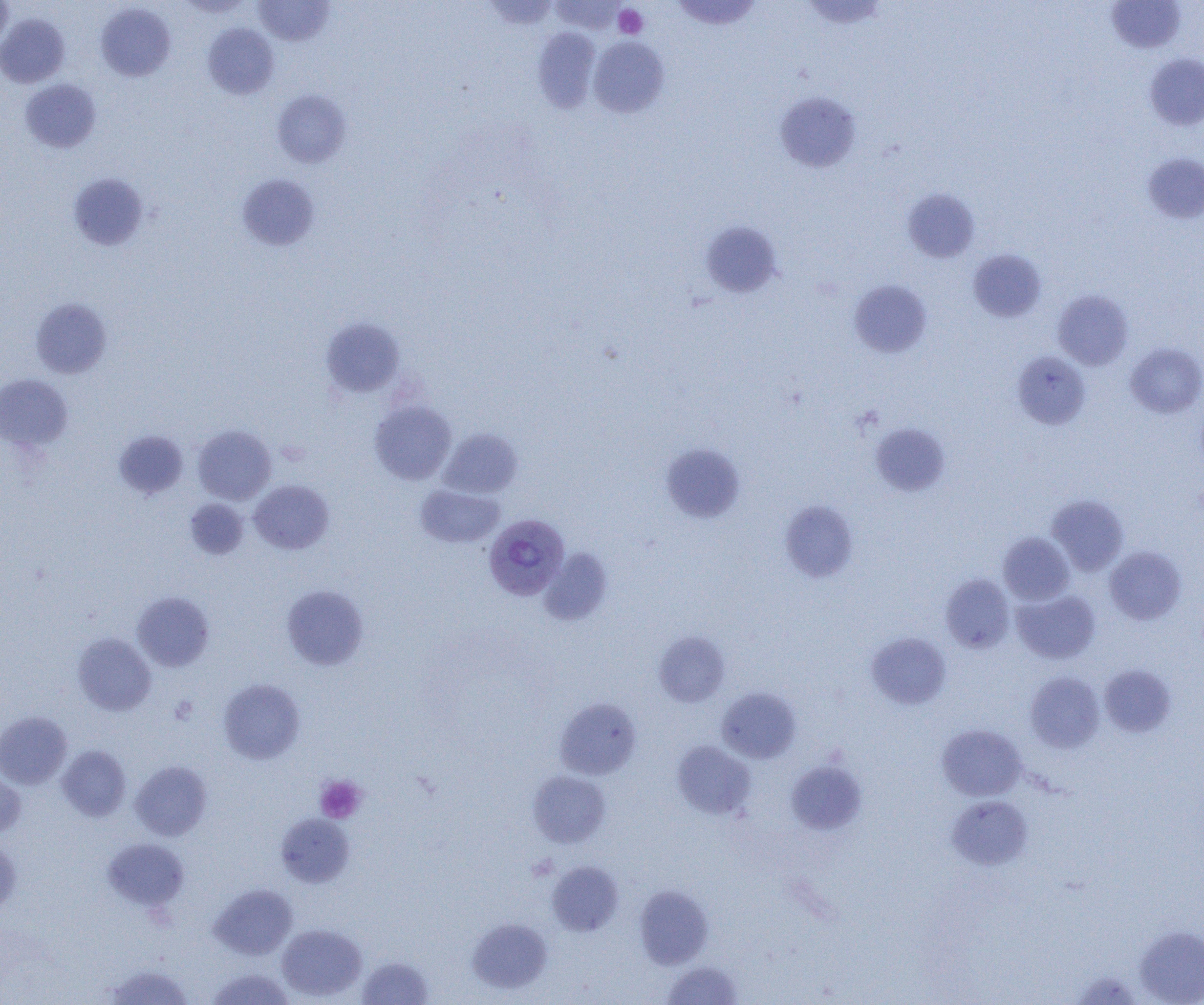

Approximate bounding boxes as [x1, y1, x2, y2] in pixels. Uninfected red blood cell locations: [0, 0, 14, 51], [177, 0, 254, 17], [549, 0, 627, 34], [671, 0, 762, 30], [801, 0, 889, 30], [253, 1, 335, 46], [1107, 1, 1186, 53], [95, 3, 175, 81], [0, 13, 70, 87], [203, 23, 278, 99], [532, 28, 601, 112], [589, 36, 669, 118], [1144, 53, 1204, 131], [20, 79, 101, 153], [271, 90, 352, 168], [775, 92, 861, 172], [1142, 152, 1204, 224], [68, 172, 149, 251], [236, 173, 320, 251], [902, 188, 979, 263], [700, 221, 783, 298], [968, 248, 1046, 322], [850, 280, 932, 357], [1053, 290, 1133, 370], [30, 297, 112, 378], [321, 318, 405, 397], [1126, 342, 1204, 417], [1013, 351, 1090, 429], [0, 374, 73, 451], [370, 400, 456, 484], [871, 423, 949, 496], [192, 425, 276, 504], [438, 428, 523, 498], [114, 430, 188, 499], [660, 443, 744, 523], [249, 480, 334, 554], [415, 484, 504, 548], [1047, 495, 1128, 575], [185, 499, 249, 560], [780, 501, 858, 582], [998, 532, 1075, 605], [1104, 546, 1186, 625], [539, 548, 612, 625], [940, 574, 1014, 653], [281, 585, 368, 669], [1012, 589, 1101, 664], [132, 592, 214, 672], [654, 631, 730, 707], [866, 632, 951, 709], [73, 633, 156, 715], [1099, 665, 1176, 737], [1025, 671, 1104, 752], [218, 678, 305, 763], [717, 687, 801, 763], [555, 698, 641, 780], [0, 711, 72, 789], [937, 724, 1026, 801], [672, 741, 756, 819], [57, 745, 131, 821], [130, 760, 212, 841], [786, 761, 866, 834], [0, 769, 26, 839], [528, 770, 611, 848], [947, 796, 1032, 870], [276, 813, 355, 887], [103, 838, 188, 911], [0, 840, 20, 916], [547, 861, 623, 936], [209, 884, 297, 960], [634, 885, 713, 969], [467, 919, 552, 993], [277, 924, 366, 1001], [1134, 925, 1204, 1004], [358, 956, 433, 1004], [661, 960, 743, 1004], [102, 962, 193, 1005], [207, 968, 295, 1005]. Plasmodium vivax-infected red blood cell locations: [484, 514, 570, 600]. Platelet locations: [614, 5, 648, 38], [170, 696, 198, 724], [315, 776, 365, 823]. Slide-level diagnosis: Plasmodium vivax. Light microscopy. Captured at 1000x magnification. One field of a larger specimen. Thin blood smear. Image is 1204×1005 pixels.